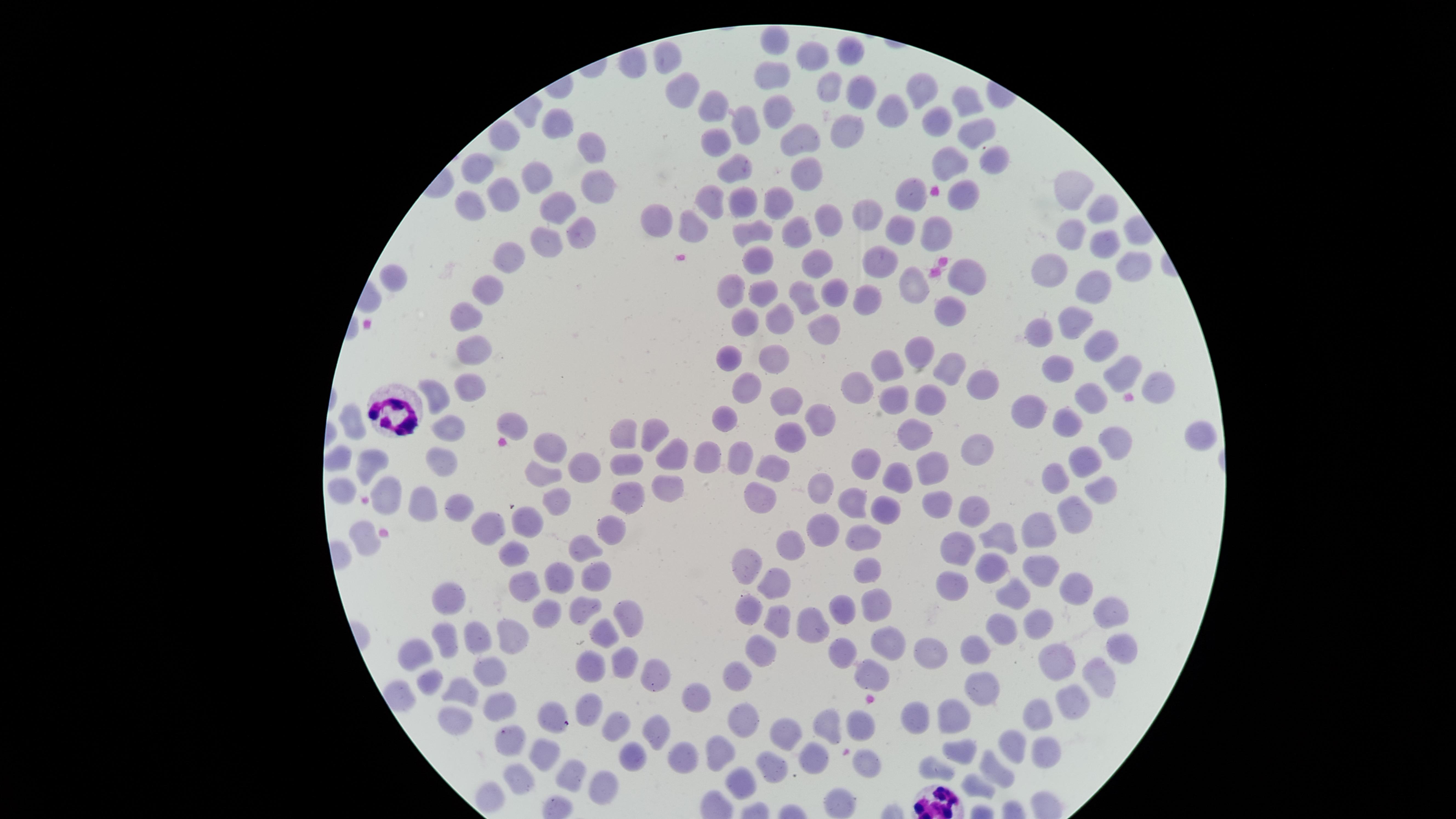 Approximate marker points, in pixels from the top-left corner. White blood cells: (x=402, y=409), (x=937, y=805). Uninfected red blood cells: (x=776, y=40), (x=847, y=51), (x=667, y=52), (x=809, y=58), (x=772, y=71), (x=827, y=88), (x=921, y=90), (x=679, y=92), (x=857, y=92), (x=968, y=102), (x=714, y=106), (x=891, y=111), (x=780, y=112), (x=555, y=119), (x=937, y=121), (x=741, y=127), (x=846, y=129), (x=977, y=130), (x=504, y=137), (x=716, y=140), (x=807, y=141), (x=596, y=148), (x=991, y=163), (x=949, y=165), (x=479, y=168), (x=733, y=172), (x=805, y=172), (x=538, y=179), (x=601, y=185), (x=1072, y=188), (x=710, y=194), (x=498, y=195), (x=780, y=195), (x=915, y=195), (x=963, y=195), (x=744, y=197), (x=471, y=207), (x=559, y=211), (x=1099, y=213), (x=869, y=214), (x=832, y=216), (x=661, y=221), (x=793, y=227), (x=900, y=229), (x=694, y=230), (x=579, y=233), (x=755, y=233), (x=937, y=233), (x=1074, y=233), (x=545, y=241), (x=1104, y=241), (x=508, y=257), (x=758, y=257), (x=881, y=257), (x=815, y=263), (x=1138, y=268), (x=1053, y=269), (x=966, y=274), (x=395, y=279), (x=1092, y=280), (x=912, y=285), (x=832, y=288), (x=489, y=289), (x=730, y=290), (x=767, y=292), (x=799, y=293), (x=870, y=299), (x=954, y=308), (x=471, y=313), (x=745, y=318), (x=779, y=318), (x=1075, y=320), (x=826, y=328), (x=1037, y=331), (x=1098, y=348), (x=477, y=351), (x=922, y=352), (x=773, y=354), (x=728, y=356), (x=889, y=364), (x=949, y=365), (x=1060, y=365), (x=1116, y=372), (x=981, y=385), (x=1164, y=385), (x=744, y=386), (x=469, y=388), (x=862, y=388), (x=435, y=395), (x=1092, y=396), (x=929, y=398), (x=896, y=399), (x=791, y=404), (x=1026, y=409), (x=510, y=418), (x=723, y=418), (x=821, y=418), (x=1070, y=418), (x=447, y=425), (x=357, y=428), (x=626, y=432), (x=661, y=432), (x=913, y=432), (x=1200, y=435), (x=789, y=438), (x=1114, y=439), (x=548, y=445), (x=981, y=446), (x=672, y=451), (x=709, y=451), (x=739, y=453), (x=1083, y=457), (x=339, y=458), (x=441, y=458), (x=864, y=462), (x=586, y=463), (x=368, y=464), (x=627, y=464), (x=775, y=464), (x=934, y=465), (x=1061, y=471), (x=539, y=477), (x=897, y=478), (x=387, y=484), (x=820, y=484), (x=663, y=486), (x=1102, y=489), (x=341, y=491), (x=624, y=496), (x=558, y=501), (x=758, y=501), (x=853, y=502), (x=939, y=502), (x=973, y=503), (x=460, y=507), (x=418, y=510), (x=884, y=512), (x=1077, y=513), (x=531, y=517), (x=825, y=529), (x=494, y=530), (x=612, y=530), (x=1041, y=533), (x=862, y=535), (x=364, y=536), (x=1001, y=536), (x=794, y=541), (x=585, y=545), (x=959, y=547), (x=512, y=550), (x=992, y=561), (x=747, y=562), (x=560, y=570), (x=1041, y=570), (x=870, y=571), (x=950, y=576), (x=595, y=578), (x=774, y=580), (x=518, y=582), (x=1076, y=590), (x=452, y=595), (x=1011, y=598), (x=875, y=601), (x=585, y=606), (x=843, y=607), (x=1109, y=607), (x=540, y=612), (x=753, y=615), (x=631, y=618), (x=813, y=619), (x=1039, y=619), (x=779, y=623), (x=607, y=631), (x=1000, y=631), (x=476, y=633), (x=446, y=637), (x=508, y=637), (x=886, y=645), (x=1120, y=645), (x=843, y=650), (x=929, y=650), (x=977, y=650), (x=418, y=652), (x=762, y=652), (x=625, y=660), (x=1063, y=662), (x=593, y=664), (x=489, y=670), (x=877, y=673), (x=739, y=677), (x=1100, y=677), (x=657, y=678), (x=427, y=680), (x=979, y=682), (x=463, y=692), (x=693, y=701), (x=1071, y=704), (x=500, y=705), (x=590, y=706), (x=912, y=715), (x=954, y=715), (x=1045, y=716), (x=554, y=720), (x=831, y=721), (x=743, y=722), (x=618, y=723), (x=455, y=724), (x=861, y=725), (x=790, y=731), (x=659, y=733), (x=504, y=739), (x=724, y=743), (x=1015, y=743), (x=965, y=755), (x=1051, y=755), (x=814, y=757), (x=542, y=758), (x=632, y=758), (x=682, y=758), (x=864, y=763), (x=778, y=764), (x=995, y=769), (x=936, y=772), (x=567, y=777), (x=513, y=779), (x=745, y=784), (x=983, y=785), (x=600, y=791), (x=487, y=798), (x=839, y=802). Image is 1456×819 pixels. One field of view of the specimen. Smartphone photograph through the microscope eyepiece. Circular visible region. Giemsa stain. Presence: no malaria parasites identified. Thin blood smear.